Assess the morphology of the red blood cells.
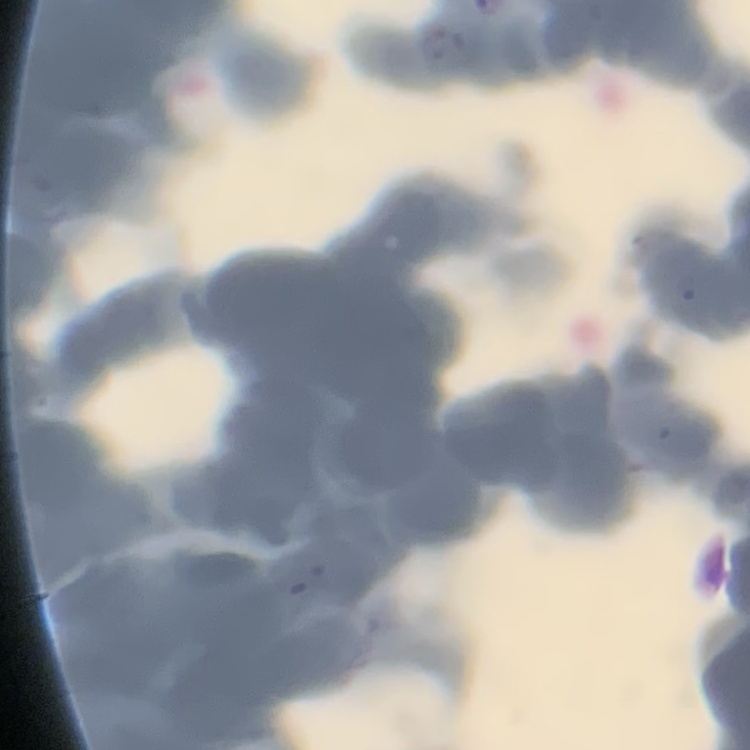

Rouleaux formation.

Stained with either Field's or Giemsa. Thin blood film. One tile cut from a larger photomicrograph.